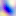

{
  "magnification": "400x",
  "identification": "Toxoplasma gondii",
  "modality": "micrograph"
}